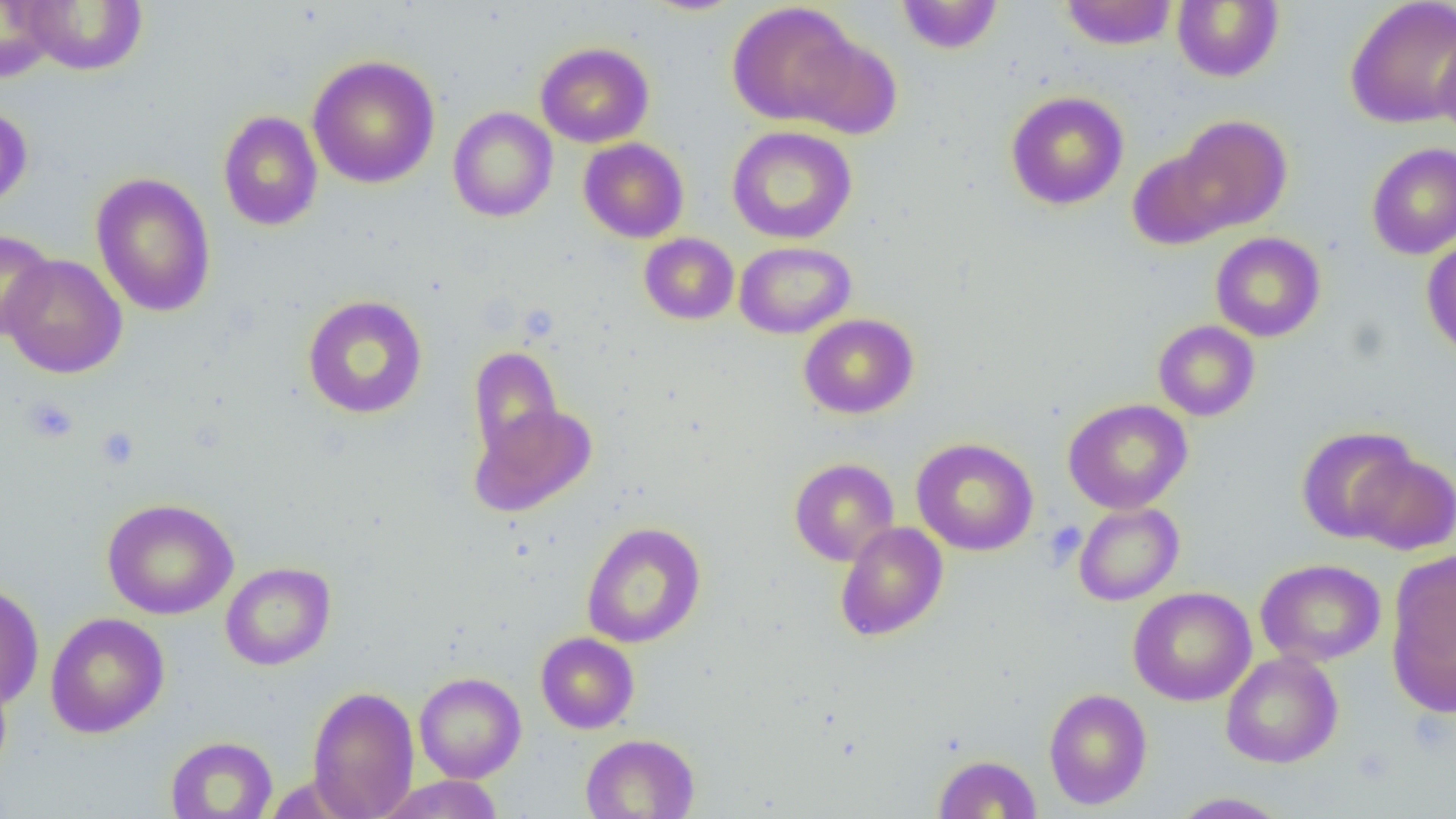
slide-level diagnosis = negative for blood parasites
field of view = single
magnification = 1000x
uninfected red blood cell locations = approximate bounding boxes as named x1/y1/x2/y2 corners in pixels: (x1=16, y1=0, x2=148, y2=75), (x1=896, y1=0, x2=1003, y2=54), (x1=1060, y1=0, x2=1178, y2=50), (x1=1345, y1=0, x2=1456, y2=129), (x1=0, y1=1, x2=58, y2=82), (x1=642, y1=1, x2=746, y2=16), (x1=1172, y1=1, x2=1283, y2=82), (x1=726, y1=2, x2=860, y2=126), (x1=1434, y1=23, x2=1456, y2=141), (x1=794, y1=33, x2=903, y2=140), (x1=535, y1=42, x2=655, y2=147), (x1=307, y1=55, x2=440, y2=189), (x1=1006, y1=91, x2=1129, y2=210), (x1=0, y1=104, x2=33, y2=211), (x1=447, y1=106, x2=558, y2=222), (x1=218, y1=110, x2=323, y2=231), (x1=1174, y1=115, x2=1292, y2=233), (x1=727, y1=125, x2=857, y2=245), (x1=578, y1=138, x2=689, y2=243), (x1=1366, y1=142, x2=1456, y2=259), (x1=1128, y1=146, x2=1235, y2=250), (x1=90, y1=172, x2=216, y2=318), (x1=0, y1=229, x2=56, y2=342), (x1=1210, y1=232, x2=1326, y2=342), (x1=639, y1=233, x2=739, y2=325), (x1=1422, y1=237, x2=1456, y2=361), (x1=734, y1=241, x2=856, y2=339), (x1=2, y1=253, x2=127, y2=379), (x1=302, y1=295, x2=428, y2=419), (x1=798, y1=313, x2=919, y2=419), (x1=1153, y1=320, x2=1260, y2=421), (x1=468, y1=347, x2=563, y2=459), (x1=1063, y1=398, x2=1193, y2=514), (x1=469, y1=403, x2=597, y2=516), (x1=1296, y1=426, x2=1418, y2=542), (x1=912, y1=437, x2=1038, y2=556), (x1=1350, y1=450, x2=1456, y2=555), (x1=789, y1=458, x2=899, y2=566), (x1=102, y1=498, x2=238, y2=619), (x1=1073, y1=502, x2=1184, y2=606), (x1=581, y1=521, x2=706, y2=649), (x1=834, y1=521, x2=948, y2=641), (x1=1255, y1=558, x2=1386, y2=667), (x1=221, y1=561, x2=336, y2=670), (x1=1386, y1=562, x2=1455, y2=715), (x1=0, y1=582, x2=45, y2=709), (x1=1128, y1=586, x2=1256, y2=706), (x1=45, y1=612, x2=170, y2=738), (x1=535, y1=632, x2=639, y2=734), (x1=1221, y1=650, x2=1343, y2=768), (x1=0, y1=669, x2=13, y2=782), (x1=414, y1=672, x2=526, y2=783), (x1=307, y1=685, x2=420, y2=818), (x1=1043, y1=688, x2=1153, y2=809), (x1=580, y1=733, x2=700, y2=819), (x1=165, y1=735, x2=278, y2=819), (x1=933, y1=754, x2=1042, y2=818), (x1=378, y1=774, x2=505, y2=818), (x1=1169, y1=792, x2=1291, y2=818)
image size = 1456×819 pixels
modality = optical microscopy
preparation = thin blood smear
platelet locations = approximate bounding boxes as named x1/y1/x2/y2 corners in pixels: (x1=21, y1=395, x2=79, y2=444), (x1=96, y1=426, x2=139, y2=469), (x1=1044, y1=520, x2=1086, y2=566)